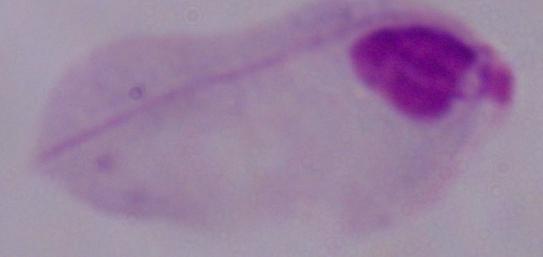
1000x magnification. A trichomonad is seen. Photomicrograph.